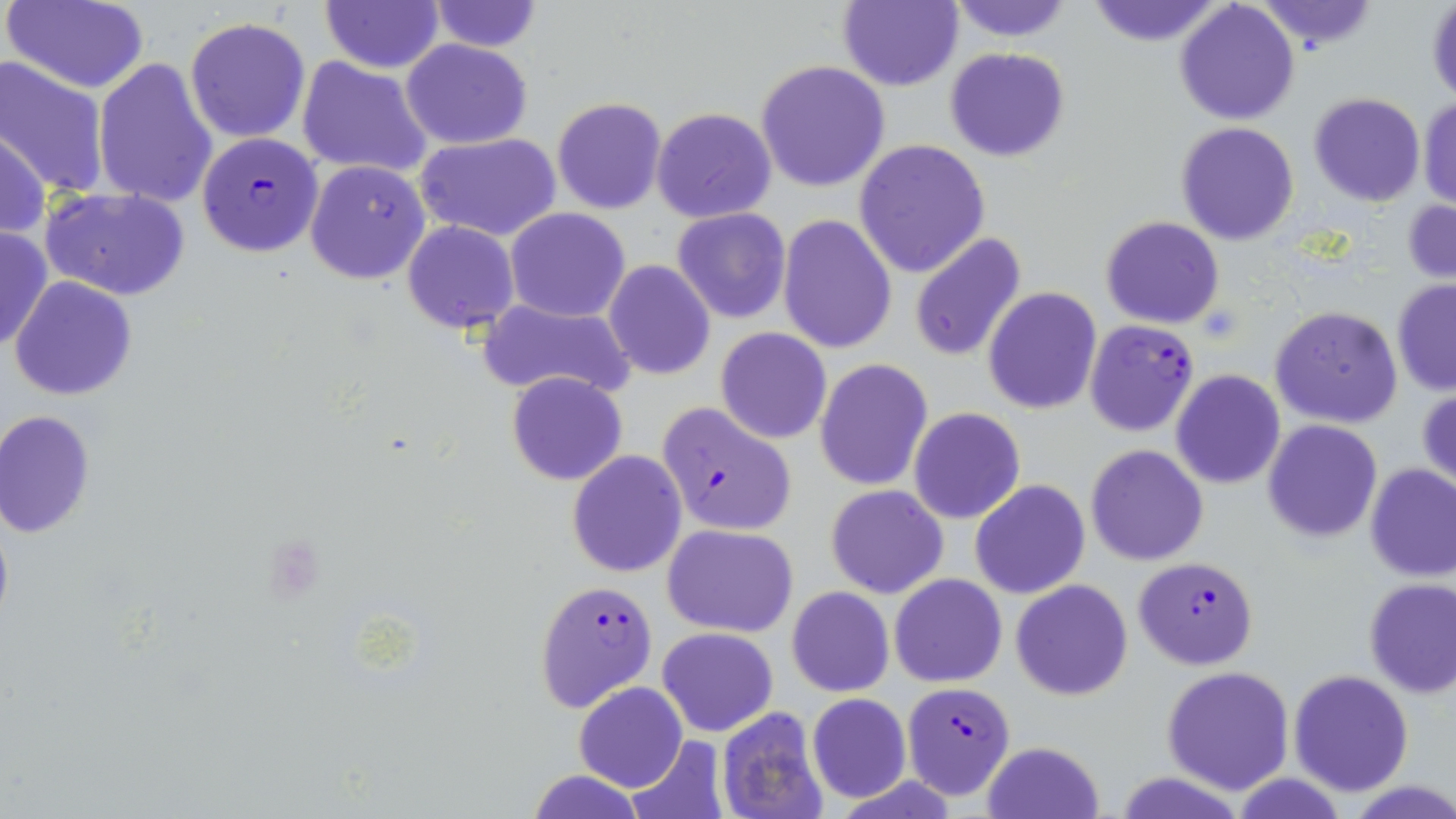
Summary:
  - Coordinate format: approximate bounding boxes as (x1,y1)-(x2,y2) corner pairs in pixels
  - Uninfected red blood cell locations: (6,0)-(151,93), (320,0)-(445,72), (427,0)-(544,53), (838,0)-(964,91), (946,0)-(1075,42), (1253,0)-(1380,53), (1082,1)-(1227,47), (1173,2)-(1301,125), (1426,2)-(1456,106), (185,17)-(310,142), (400,39)-(533,151), (944,46)-(1070,162), (0,55)-(113,200), (298,57)-(433,180), (93,58)-(218,207), (757,59)-(890,192), (1307,92)-(1428,207), (552,97)-(669,216), (1417,98)-(1455,209), (652,107)-(777,224), (1175,121)-(1300,246), (0,126)-(49,242), (415,133)-(562,241), (853,140)-(990,277), (305,158)-(431,285), (45,187)-(190,299), (1402,199)-(1456,285), (505,207)-(630,322), (672,208)-(792,323), (777,214)-(898,354), (1099,216)-(1225,329), (402,221)-(519,334), (0,225)-(52,353), (909,233)-(1027,362), (604,260)-(715,381), (9,276)-(138,402), (1390,279)-(1456,394), (983,288)-(1102,413), (476,300)-(636,404), (1269,306)-(1402,428), (715,328)-(832,444), (814,359)-(933,491), (1172,370)-(1286,490), (506,372)-(629,487), (1418,386)-(1456,492), (908,407)-(1026,525), (0,409)-(96,538), (1262,420)-(1383,541), (1086,444)-(1209,566), (567,451)-(688,576), (1364,463)-(1456,583), (970,480)-(1089,600), (825,483)-(948,598), (662,522)-(800,637), (891,574)-(1006,687), (1011,578)-(1132,701), (1362,578)-(1456,697), (786,586)-(894,696), (657,626)-(779,737), (623,635)-(767,800), (1162,666)-(1295,793), (1288,668)-(1414,796), (574,682)-(688,792), (807,693)-(911,804), (715,708)-(832,819), (625,736)-(730,819), (984,739)-(1103,819), (529,770)-(644,818)
  - Plasmodium falciparum-infected red blood cell locations: (196,132)-(325,258), (1084,319)-(1200,437), (655,400)-(799,538), (1132,556)-(1260,669), (536,579)-(658,711), (902,681)-(1015,798)
  - Slide-level diagnosis: Plasmodium falciparum
  - Image size: 1456×819 pixels
  - Magnification: 1000x
  - Field of view: single
  - Modality: light microscopy
  - Preparation: thin blood smear
  - Stain: May-Grünwald-Giemsa